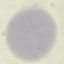

malaria status = uninfected
image type = automatically extracted cell patch, resized to 64 × 64 pixels
capture = smartphone through the microscope eyepiece
preparation = thin blood smear
stain = Giemsa